Assess the morphology of the red blood cells.
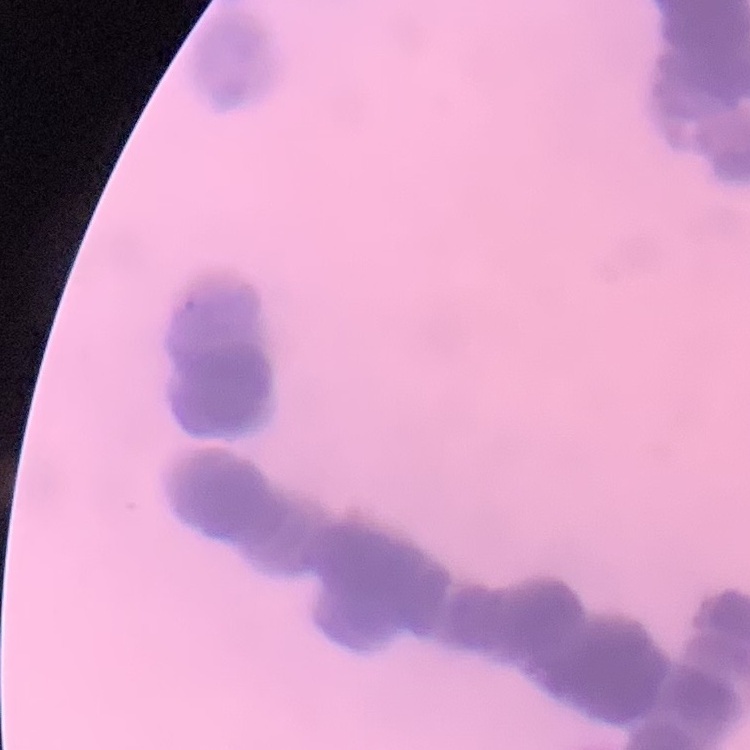

They show rouleaux formation.

Summary:
  - Stain: Field's or Giemsa
  - Image type: one tile cut from a larger photomicrograph
  - Preparation: thin blood smear